Name the parasite shown.
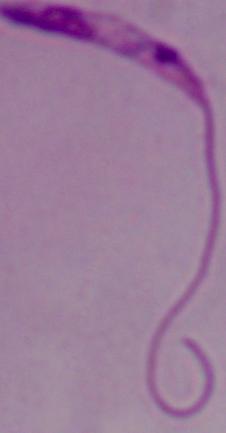

Leishmania.

Summary:
  - Modality: micrograph
  - Magnification: 1000x